Classify the preparation.
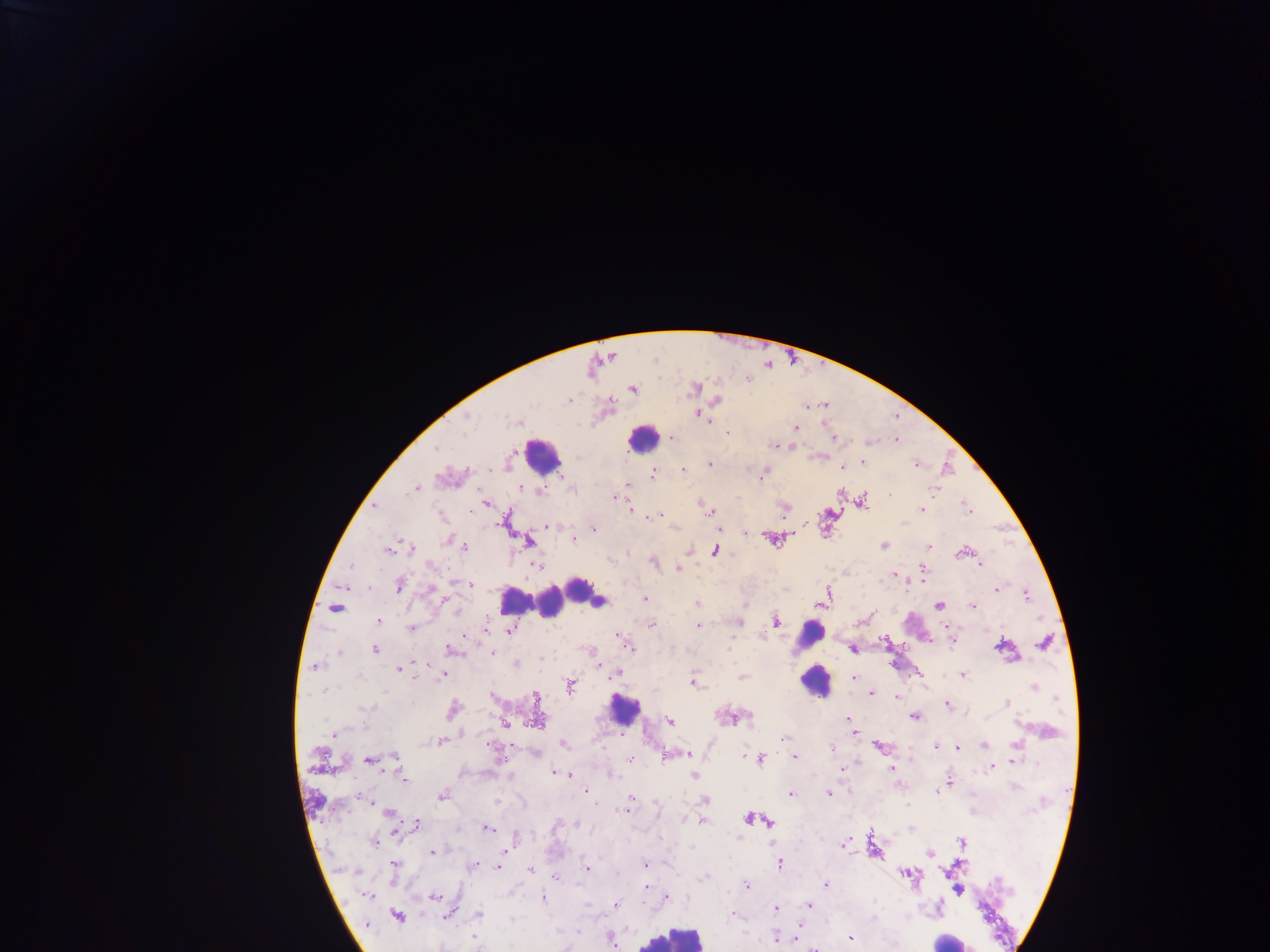
Thick blood film.

capture = mobile-phone photograph through a microscope
leukocyte locations = approximate centers as [x, y] in pixels (subset; some below the resolvable size): [640, 439], [545, 459], [577, 587], [515, 601], [550, 606], [807, 636], [814, 687], [620, 708], [675, 936], [948, 939]
malaria parasite locations = approximate centers as [x, y] in pixels: [654, 360], [632, 389], [609, 401], [697, 412], [896, 418], [710, 423], [825, 425], [794, 427], [671, 438], [834, 439], [894, 442], [774, 447], [793, 448], [436, 449], [819, 457], [863, 463], [710, 464], [916, 464], [686, 471], [655, 474], [761, 474], [414, 488], [935, 489], [522, 491], [890, 495], [614, 497], [484, 505], [376, 506], [965, 507], [783, 508], [631, 511], [922, 511], [708, 512], [648, 519], [665, 521], [803, 524], [546, 526], [673, 527], [594, 530], [744, 534], [572, 539], [445, 540], [529, 542], [884, 544], [928, 546], [465, 547], [385, 550], [413, 550], [688, 550], [958, 553], [653, 560], [431, 565], [539, 565], [980, 566], [923, 567], [678, 568], [894, 575], [911, 583], [471, 584], [399, 585], [428, 588], [996, 590], [1025, 595], [643, 598], [598, 601], [696, 603], [940, 607], [973, 607], [455, 612], [871, 613], [377, 622], [739, 622], [653, 623], [698, 626], [950, 627], [410, 629], [485, 630], [510, 631], [467, 635], [830, 635], [762, 637], [881, 638], [951, 641], [627, 646], [853, 649], [376, 651], [457, 652], [494, 653], [515, 663], [597, 663], [316, 668], [399, 670], [443, 674], [963, 675], [359, 676], [741, 677], [418, 678], [614, 678], [853, 678], [694, 683], [871, 695], [897, 696], [1007, 703], [948, 704], [637, 706], [365, 708], [914, 717], [849, 718], [671, 721], [731, 721], [333, 732], [853, 733], [465, 734], [784, 738], [440, 741], [563, 743], [935, 745], [878, 747], [830, 748], [957, 749], [685, 754], [743, 756], [667, 757], [796, 757], [395, 758], [761, 758], [367, 759], [629, 759], [892, 768], [843, 770], [553, 773], [568, 774], [694, 774], [405, 780], [949, 783], [584, 790], [791, 793], [827, 793], [358, 796], [442, 797], [630, 797], [705, 800], [369, 802], [596, 805], [904, 805], [388, 812], [621, 812], [626, 813], [683, 816], [746, 819], [702, 822], [769, 823], [575, 824], [416, 825], [487, 829], [397, 834], [738, 837], [372, 844], [843, 844], [431, 852], [505, 852], [394, 864], [644, 864], [475, 865], [782, 866], [497, 868], [586, 868], [529, 869], [356, 871], [746, 884], [826, 884], [644, 887], [369, 897], [668, 897], [434, 898], [544, 899], [615, 905], [809, 906], [773, 909], [477, 914], [449, 916], [577, 932], [472, 936], [774, 939], [851, 939], [610, 941], [811, 948]
image size = 1270×952 pixels
field of view = single
country = Ghana